Classify this cell by malaria status.
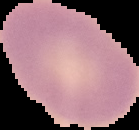
Uninfected.

Summary:
  - Preparation: thin blood smear
  - Image type: cell region segmented out of the field of view; surrounding area masked to black
  - Image size: 139×130 pixels